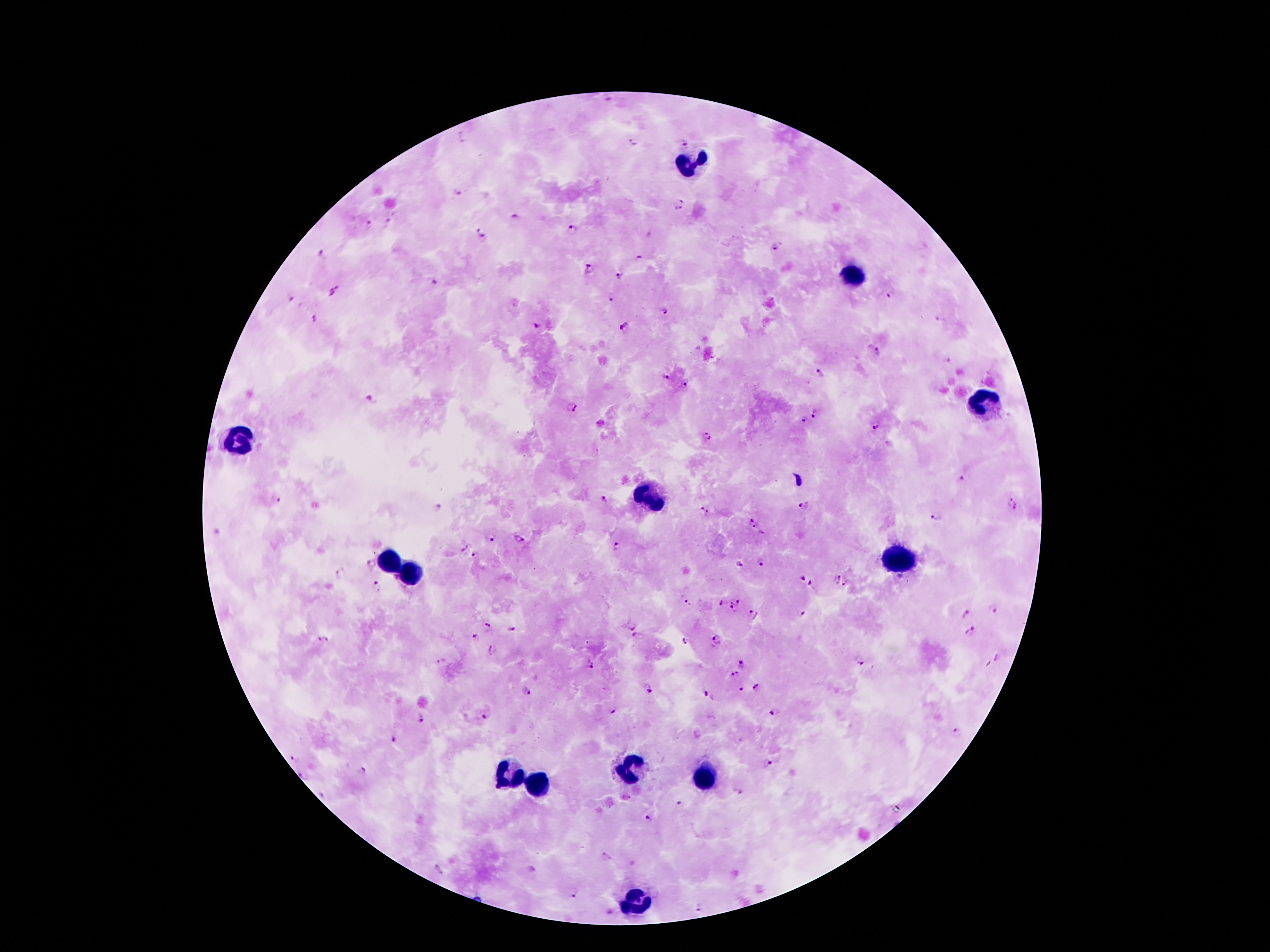

{
  "field_of_view": "single",
  "leukocyte_locations": "approximate centers as {x, y} in pixels: {686, 164}, {852, 276}, {983, 399}, {240, 438}, {647, 497}, {897, 559}, {392, 562}, {410, 574}, {627, 767}, {507, 769}, {704, 778}, {534, 785}, {633, 900}",
  "malaria_parasite_locations": "approximate centers as {x, y} in pixels: {634, 142}, {684, 142}, {457, 191}, {682, 200}, {678, 209}, {516, 217}, {387, 221}, {369, 224}, {572, 231}, {481, 234}, {774, 247}, {324, 252}, {638, 257}, {589, 269}, {619, 276}, {434, 282}, {334, 291}, {891, 294}, {612, 297}, {291, 298}, {665, 311}, {939, 317}, {314, 318}, {538, 325}, {623, 326}, {878, 353}, {948, 360}, {820, 373}, {665, 375}, {686, 385}, {371, 400}, {571, 406}, {815, 413}, {803, 420}, {600, 424}, {877, 426}, {708, 436}, {962, 480}, {275, 499}, {604, 500}, {1009, 500}, {804, 505}, {437, 506}, {1017, 507}, {704, 512}, {936, 517}, {753, 523}, {217, 533}, {763, 535}, {491, 536}, {519, 539}, {462, 544}, {616, 547}, {475, 558}, {761, 562}, {370, 565}, {739, 565}, {341, 575}, {899, 576}, {801, 578}, {837, 578}, {811, 583}, {379, 586}, {846, 586}, {736, 599}, {687, 603}, {722, 604}, {994, 608}, {732, 609}, {966, 613}, {753, 614}, {800, 614}, {489, 623}, {630, 624}, {511, 629}, {970, 631}, {324, 637}, {639, 637}, {476, 638}, {716, 638}, {686, 641}, {492, 650}, {999, 658}, {442, 660}, {742, 664}, {590, 665}, {860, 665}, {735, 675}, {756, 690}, {646, 691}, {740, 691}, {527, 692}, {707, 694}, {613, 712}, {774, 712}, {485, 717}, {422, 718}, {956, 734}, {394, 739}, {295, 760}, {768, 764}, {362, 772}, {303, 775}, {740, 792}, {326, 794}, {679, 803}, {648, 819}, {606, 856}, {440, 868}, {573, 894}, {698, 907}, {610, 910}",
  "magnification": "100x",
  "image_size": "1270×952 pixels",
  "stain": "Giemsa",
  "patient_malaria_status": "infected with Plasmodium falciparum",
  "capture": "smartphone through the microscope eyepiece",
  "preparation": "thick blood smear"
}